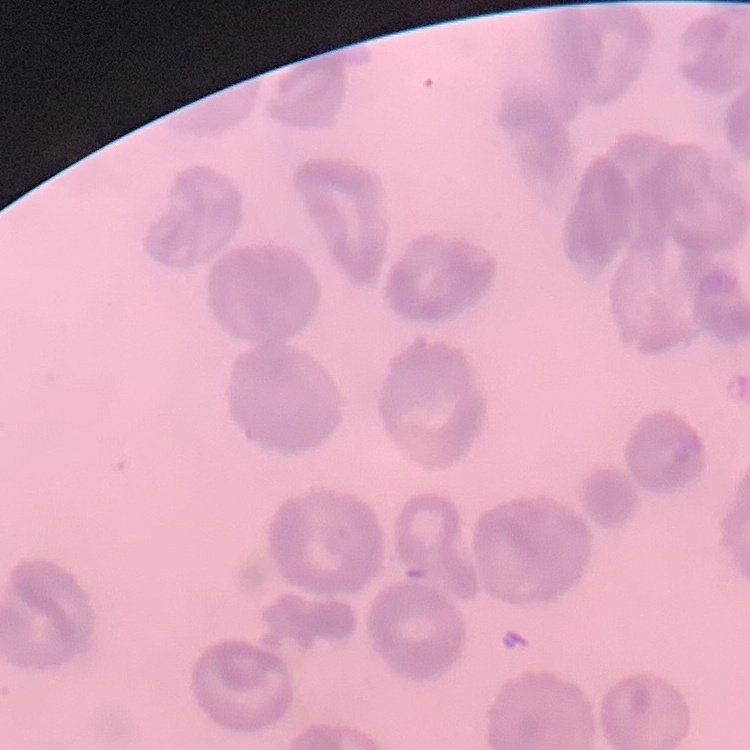

The erythrocytes exhibit no rouleaux formation. Stained with either Field's or Giemsa. Square crop of a larger photomicrograph. Thin blood smear.